Report the malaria status of this cell.
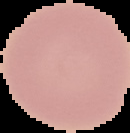
Uninfected.

image type = segmented cell region on a black background
preparation = thin blood film
image size = 130×133 pixels